Locate every Plasmodium parasite.
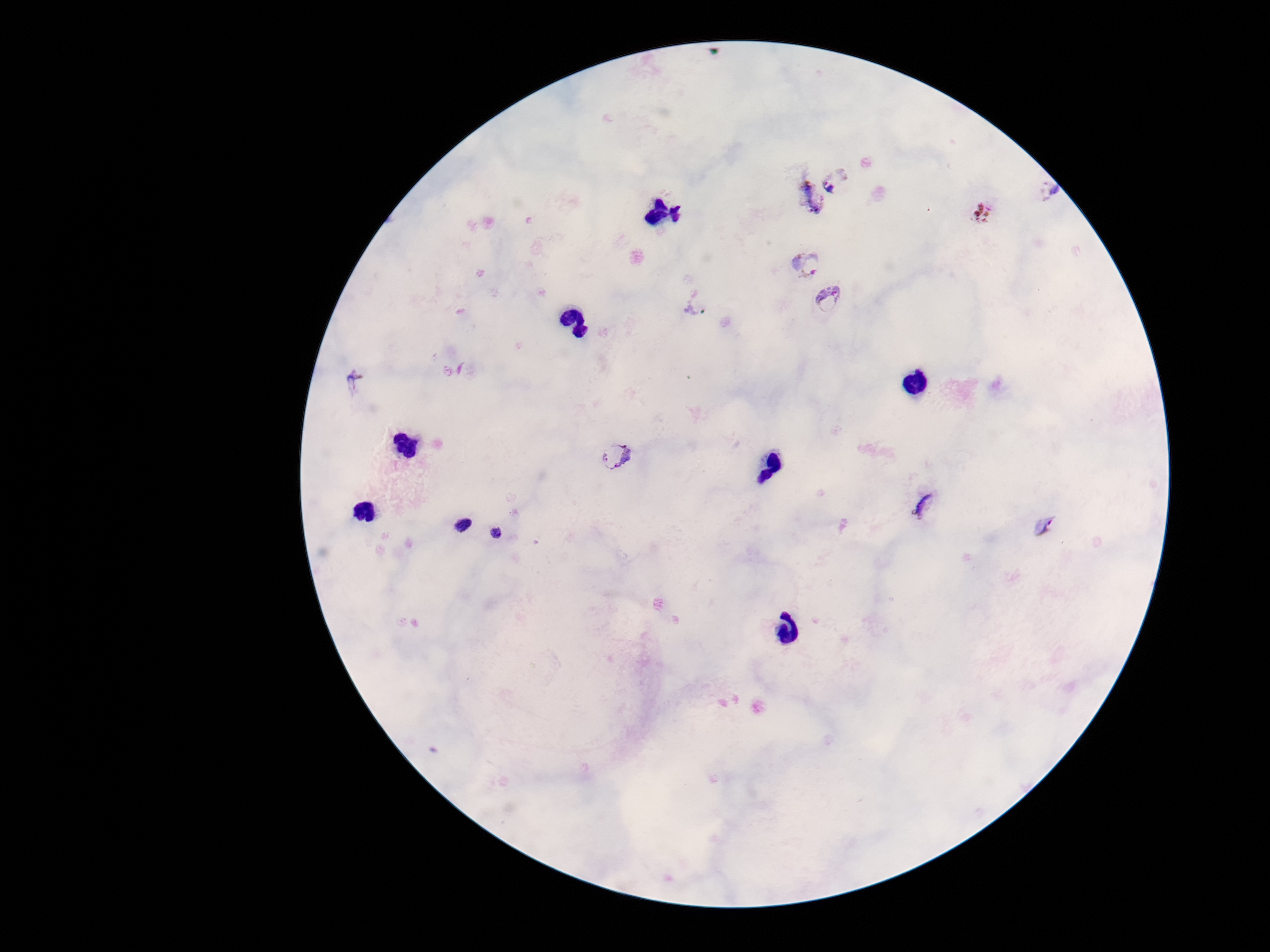

Approximate object centers, in pixels from the top-left corner.
Plasmodium parasites: (x=839, y=182), (x=1048, y=192), (x=810, y=197), (x=982, y=212), (x=809, y=263), (x=827, y=299), (x=699, y=307), (x=356, y=380), (x=618, y=455), (x=928, y=504), (x=460, y=524), (x=1044, y=526), (x=498, y=537).

patient malaria status = positive
preparation = thick peripheral-blood smear
image size = 1270×952 pixels
stain = Giemsa
capture = smartphone camera through the microscope eyepiece
field of view = one from this slide
magnification = 100x